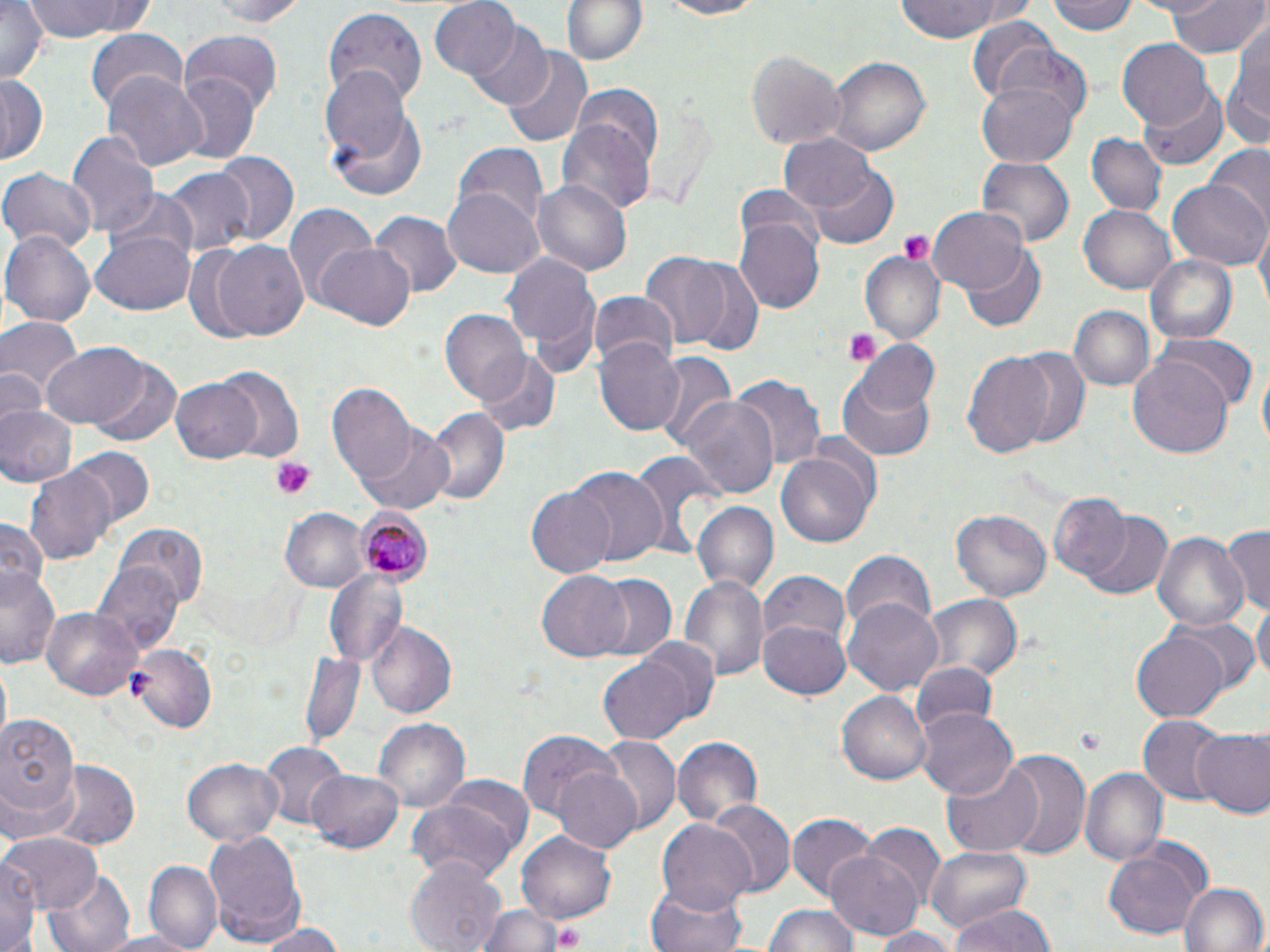

Summary:
  - Coordinate format: approximate bounding boxes as [x1, y1, x2, y2] in pixels
  - Platelet locations: [895, 229, 935, 263], [845, 331, 881, 366], [269, 457, 317, 500], [550, 921, 587, 951]
  - Plasmodium malariae-infected red blood cell locations: [351, 510, 432, 585]
  - Uninfected red blood cell locations: [0, 0, 47, 86], [23, 0, 155, 43], [210, 0, 310, 28], [558, 0, 649, 68], [649, 0, 768, 19], [893, 0, 1014, 42], [1050, 0, 1140, 36], [1168, 0, 1266, 58], [428, 1, 520, 79], [322, 8, 427, 106], [965, 17, 1060, 100], [463, 21, 554, 110], [1222, 24, 1270, 154], [86, 28, 189, 114], [179, 34, 283, 118], [1118, 40, 1214, 129], [985, 42, 1094, 137], [501, 48, 591, 148], [746, 49, 845, 150], [828, 57, 931, 159], [321, 70, 425, 198], [102, 72, 207, 173], [173, 73, 259, 166], [0, 78, 46, 163], [976, 79, 1079, 168], [1136, 82, 1228, 172], [571, 83, 662, 167], [559, 118, 654, 220], [67, 130, 158, 241], [776, 133, 879, 215], [1086, 134, 1163, 214], [453, 144, 549, 232], [1204, 145, 1270, 227], [212, 152, 300, 247], [980, 158, 1072, 246], [160, 166, 254, 258], [811, 167, 898, 248], [0, 168, 97, 257], [532, 177, 632, 278], [1169, 177, 1270, 270], [733, 182, 823, 265], [443, 185, 543, 278], [102, 189, 201, 275], [283, 203, 379, 307], [1079, 203, 1178, 294], [928, 207, 1028, 295], [370, 210, 461, 297], [736, 216, 825, 312], [1254, 224, 1269, 315], [95, 228, 196, 315], [3, 231, 94, 327], [206, 240, 309, 342], [316, 246, 414, 330], [963, 248, 1047, 332], [638, 249, 743, 353], [502, 252, 599, 358], [861, 252, 945, 343], [1146, 253, 1239, 344], [682, 258, 763, 358], [588, 291, 681, 369], [1068, 305, 1157, 390], [440, 311, 529, 405], [0, 317, 82, 403], [1150, 333, 1254, 414], [595, 339, 686, 436], [854, 339, 938, 416], [39, 340, 157, 434], [1007, 345, 1091, 448], [474, 350, 560, 436], [963, 351, 1057, 463], [649, 353, 736, 452], [1126, 354, 1236, 462], [1256, 358, 1268, 463], [87, 359, 182, 448], [215, 366, 304, 461], [0, 367, 46, 433], [837, 374, 937, 460], [731, 375, 826, 471], [170, 377, 263, 464], [328, 387, 417, 488], [676, 396, 778, 497], [0, 402, 77, 484], [423, 407, 510, 508], [356, 426, 457, 516], [71, 447, 151, 526], [774, 447, 875, 547], [629, 452, 726, 555], [24, 465, 115, 566], [567, 468, 668, 567], [527, 487, 619, 579], [1047, 493, 1131, 580], [690, 502, 780, 596], [280, 508, 370, 594], [950, 511, 1051, 601], [1077, 511, 1171, 601], [0, 516, 49, 594], [1221, 522, 1270, 617], [117, 523, 207, 607], [1153, 530, 1248, 636], [838, 549, 935, 636], [93, 563, 182, 659], [1, 564, 63, 671], [760, 568, 851, 648], [324, 571, 406, 665], [534, 571, 633, 662], [588, 574, 676, 659], [676, 574, 768, 684], [924, 595, 1023, 685], [844, 598, 943, 697], [1251, 601, 1269, 689], [42, 609, 139, 699], [1172, 617, 1258, 698], [757, 620, 851, 701], [366, 623, 456, 719], [1130, 627, 1232, 722], [627, 639, 720, 726], [126, 643, 217, 732], [299, 652, 365, 748], [598, 656, 694, 744], [910, 663, 994, 738], [837, 690, 931, 785], [918, 705, 1019, 800], [1, 713, 83, 826], [1137, 714, 1228, 804], [373, 718, 469, 811], [1193, 728, 1270, 818], [518, 731, 625, 825], [671, 736, 763, 828], [601, 737, 678, 834], [259, 742, 345, 830], [996, 750, 1091, 862], [182, 758, 284, 848], [939, 761, 1042, 855], [50, 762, 140, 850], [309, 767, 406, 853], [552, 767, 643, 853], [1080, 768, 1166, 868], [437, 778, 532, 860], [406, 799, 524, 883], [707, 800, 794, 898], [786, 812, 878, 903], [656, 819, 756, 918], [859, 825, 945, 908], [205, 829, 305, 948], [516, 831, 617, 924], [3, 832, 101, 914], [925, 845, 1031, 932], [1102, 846, 1208, 942], [826, 850, 922, 940], [1, 853, 40, 952], [405, 855, 505, 952], [146, 860, 222, 951], [43, 869, 134, 952], [1179, 882, 1266, 952], [642, 884, 752, 952], [949, 903, 1055, 952], [471, 905, 581, 952], [765, 907, 858, 952], [252, 921, 347, 951], [865, 925, 961, 952]
  - Slide-level diagnosis: Plasmodium malariae
  - Field of view: single
  - Stain: May-Grünwald-Giemsa
  - Modality: optical microscopy
  - Magnification: 1000x
  - Preparation: thin blood smear
  - Image size: 1270×952 pixels